Assess this cell for malaria.
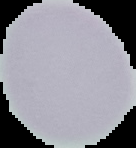
It is uninfected.

Image is 136×148 pixels. The area outside the segmented cell region is set to black. From a thin blood smear.